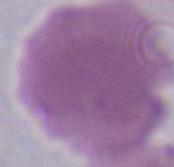
Summary:
  - Magnification: 1000x
  - Identification: erythrocyte
  - Modality: photomicrograph